Comment on the morphology of the red blood cells.
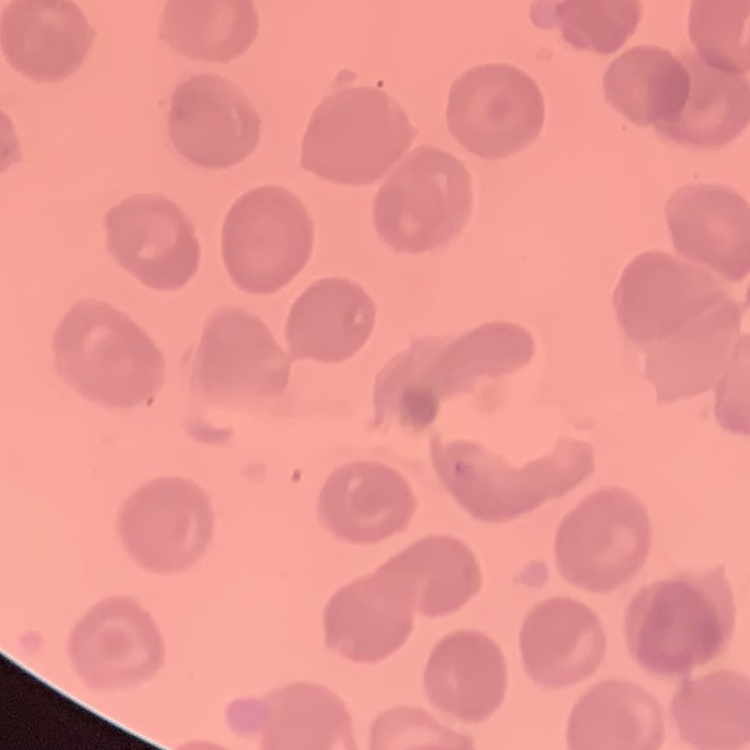
They show no rouleaux formation.

Summary:
  - Stain: Field's or Giemsa
  - Image type: one tile cut from a larger photomicrograph
  - Preparation: thin blood film